State the blood parasite species.
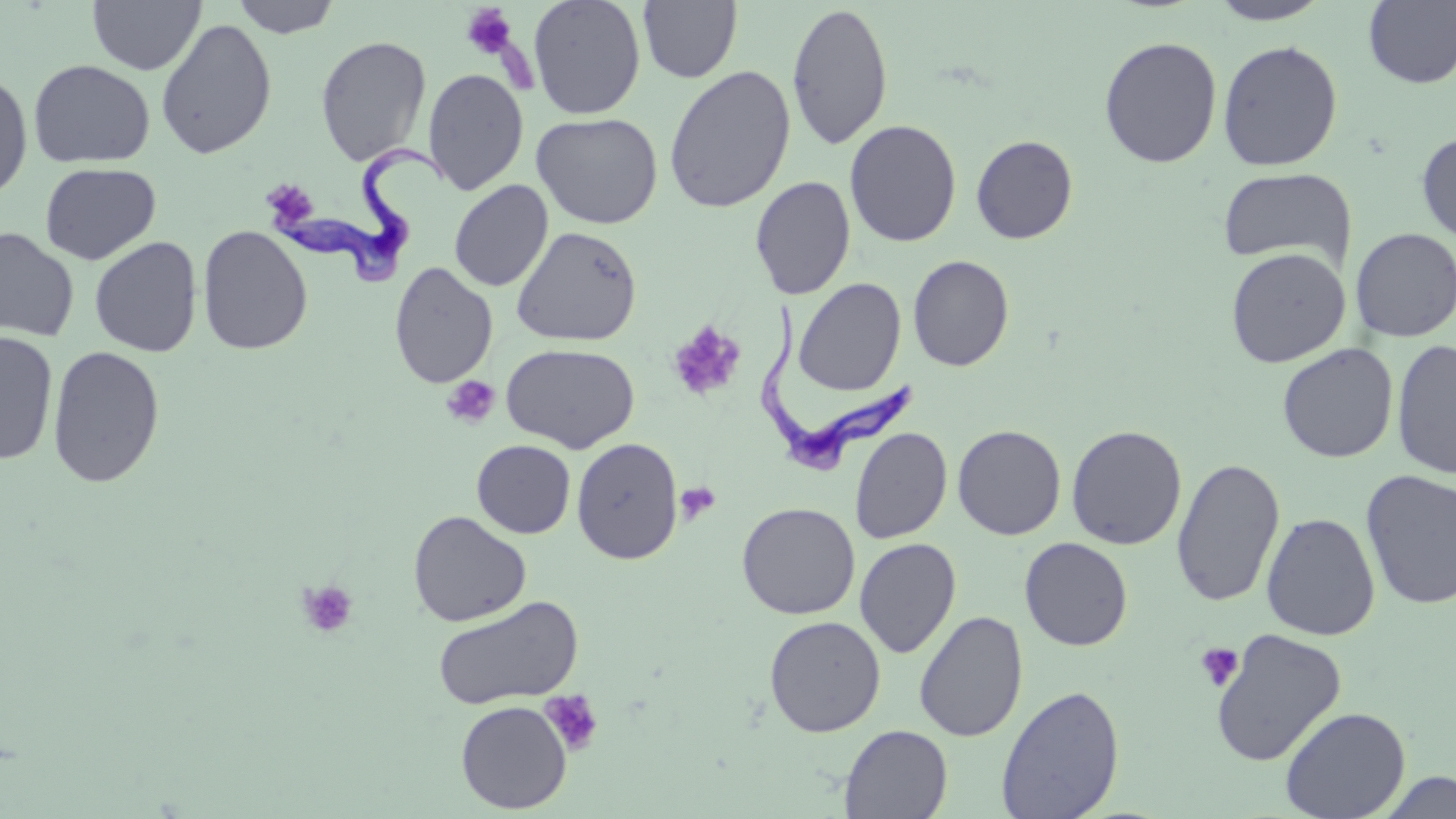

Trypanosoma brucei.

magnification: 1000x
field_of_view: one of a larger specimen
preparation: thin blood smear
image_size: 1456×819 pixels
platelet_locations: 'approximate bounding boxes as [x1, y1, x2, y2] in pixels: [461, 3, 518, 59], [261, 180, 316, 218], [667, 321, 746, 402], [441, 375, 501, 429], [674, 482, 721, 527], [297, 580, 358, 639], [1195, 642, 1244, 692], [538, 690, 604, 756]'
stain: May-Grünwald-Giemsa
modality: light microscopy
uninfected_red_blood_cell_locations: 'approximate bounding boxes as [x1, y1, x2, y2] in pixels: [87, 0, 205, 75], [230, 0, 342, 38], [528, 0, 646, 120], [1207, 0, 1333, 25], [1363, 0, 1456, 89], [638, 1, 743, 83], [786, 2, 894, 151], [156, 18, 277, 160], [315, 35, 432, 166], [1098, 36, 1222, 168], [1217, 40, 1344, 171], [28, 59, 155, 168], [663, 64, 797, 214], [0, 68, 33, 200], [423, 68, 529, 195], [531, 112, 663, 230], [844, 119, 961, 247], [1416, 130, 1456, 246], [970, 135, 1078, 244], [40, 162, 161, 265], [1217, 167, 1356, 270], [750, 175, 856, 300], [449, 180, 553, 292], [197, 226, 313, 355], [510, 226, 643, 347], [0, 228, 79, 343], [1350, 228, 1456, 341], [88, 236, 203, 357], [1226, 247, 1350, 368], [907, 255, 1014, 372], [389, 262, 498, 389], [793, 277, 907, 396], [0, 331, 59, 465], [1391, 338, 1456, 480], [500, 342, 640, 453], [1277, 343, 1399, 463], [47, 344, 165, 488], [952, 424, 1066, 540], [1066, 424, 1187, 550], [849, 427, 952, 544], [571, 437, 683, 564], [472, 440, 575, 538], [1172, 457, 1285, 608], [1360, 469, 1456, 610], [736, 502, 860, 619], [408, 511, 531, 627], [1261, 513, 1380, 640], [855, 537, 961, 658], [1019, 537, 1133, 650], [432, 595, 584, 710], [914, 610, 1028, 742], [764, 615, 886, 737], [1210, 628, 1347, 767], [995, 684, 1124, 819], [455, 700, 572, 814], [1279, 706, 1411, 819], [839, 724, 953, 819], [1372, 770, 1456, 818]'
trypanosoma_brucei_locations: 'approximate bounding boxes as [x1, y1, x2, y2] in pixels: [261, 145, 451, 287], [758, 301, 920, 479]'